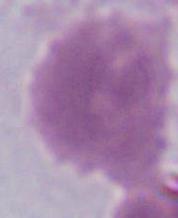
Captured at 1000x magnification. Photomicrograph. A red blood cell is shown.